Classify this cell by malaria status.
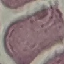

Uninfected.

image type = automatically extracted cell patch, resized to 64 × 64 pixels
stain = Giemsa
capture = smartphone through the microscope eyepiece
preparation = thin blood smear